Give the position of every Plasmodium parasite.
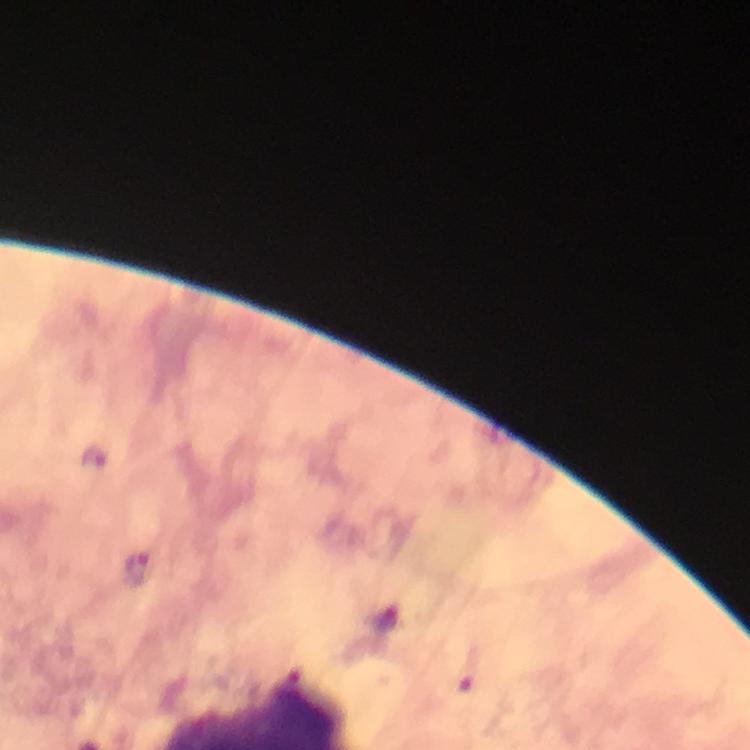

Approximate centers as (x, y) in pixels.
Plasmodium parasites: (95, 459), (139, 569), (469, 668).

Immersion oil was used. At 100x magnification. Photographed with a smartphone mounted on the microscope. Giemsa stain. From a diagnostic examination for malaria. Thick blood film. A crop from one field of view. Image is 750×750 pixels.